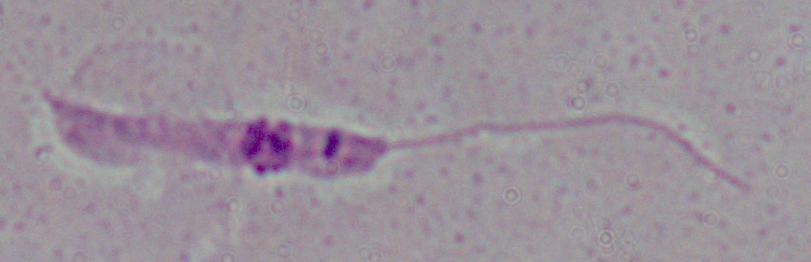
modality = photomicrograph
magnification = 1000x
identification = Leishmania